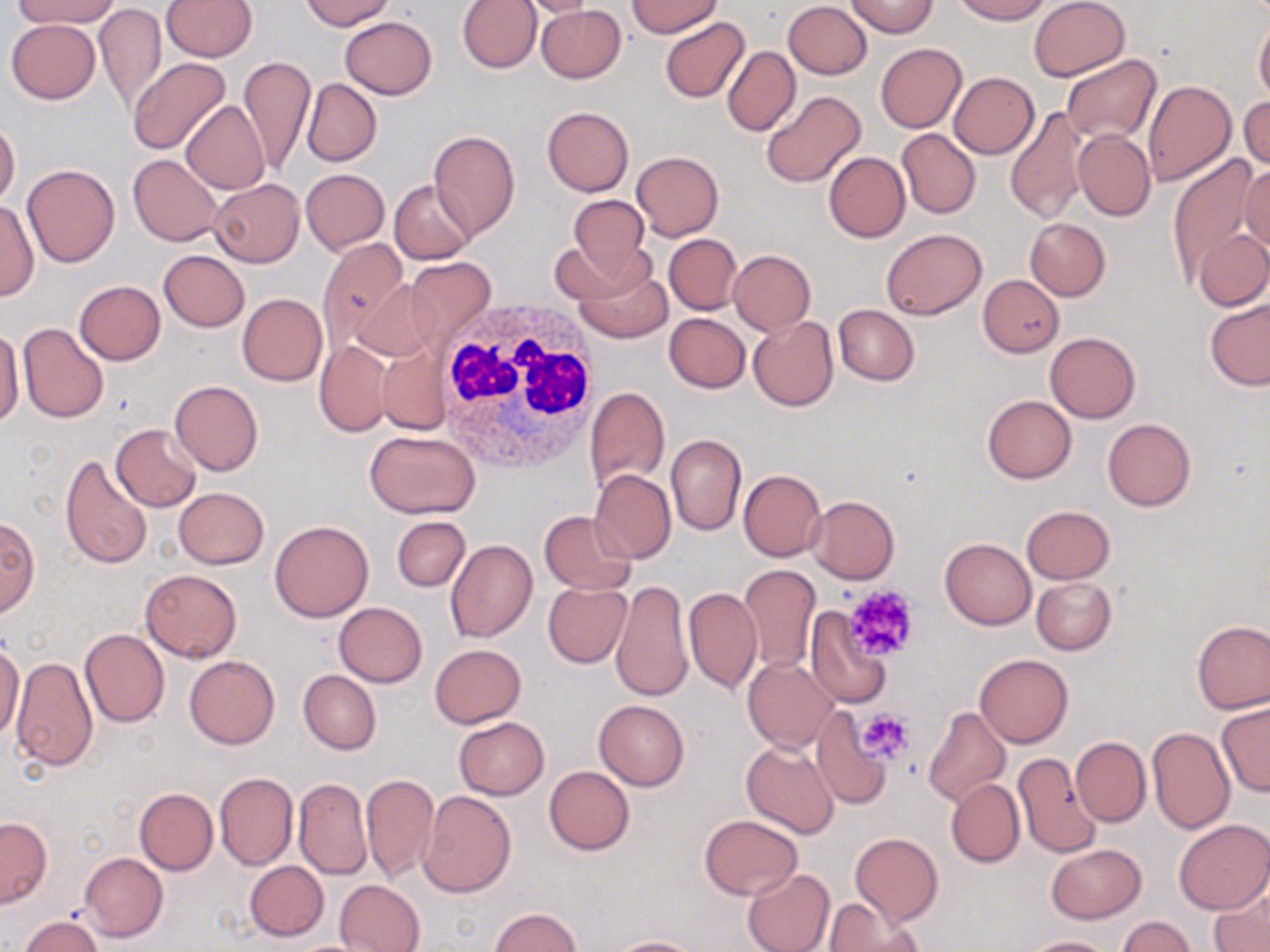
Approximate bounding boxes as [x1, y1, x2, y2] in pixels. Platelet locations: [842, 585, 920, 662], [857, 708, 914, 763]. Uninfected red blood cell locations: [13, 0, 118, 29], [162, 0, 257, 61], [302, 0, 393, 30], [457, 0, 541, 73], [518, 0, 603, 19], [627, 0, 722, 37], [952, 0, 1051, 23], [1028, 0, 1130, 82], [784, 1, 872, 79], [846, 1, 938, 37], [94, 3, 166, 113], [536, 5, 625, 82], [340, 17, 436, 99], [660, 17, 749, 103], [6, 18, 100, 103], [1255, 18, 1270, 105], [875, 43, 967, 133], [722, 46, 800, 137], [1059, 54, 1160, 145], [238, 55, 314, 175], [128, 57, 231, 156], [949, 72, 1039, 158], [302, 78, 382, 166], [1142, 79, 1237, 185], [761, 90, 866, 189], [1240, 94, 1269, 171], [182, 100, 269, 194], [1005, 106, 1091, 224], [542, 107, 634, 197], [0, 121, 20, 205], [897, 129, 980, 219], [428, 130, 520, 239], [1072, 130, 1155, 220], [632, 151, 723, 240], [823, 152, 910, 242], [129, 153, 225, 247], [1168, 158, 1258, 281], [1238, 159, 1269, 259], [22, 164, 120, 267], [301, 169, 389, 254], [210, 178, 304, 267], [390, 179, 476, 264], [566, 195, 651, 286], [0, 198, 38, 302], [1025, 218, 1110, 300], [882, 228, 985, 320], [1195, 229, 1270, 311], [664, 234, 741, 314], [318, 238, 407, 348], [549, 240, 634, 305], [159, 250, 248, 331], [728, 250, 815, 334], [404, 257, 495, 351], [575, 265, 671, 343], [978, 275, 1063, 356], [354, 278, 439, 360], [74, 281, 165, 364], [237, 293, 327, 386], [1204, 297, 1270, 390], [833, 305, 919, 386], [664, 312, 750, 392], [749, 316, 838, 411], [18, 323, 108, 422], [1, 324, 24, 426], [1044, 332, 1140, 422], [313, 339, 394, 437], [376, 347, 449, 434], [169, 379, 263, 476], [584, 386, 669, 492], [981, 395, 1076, 484], [1102, 419, 1195, 511], [110, 423, 201, 513], [364, 430, 480, 517], [666, 432, 746, 536], [60, 452, 152, 569], [738, 468, 826, 561], [589, 469, 676, 564], [173, 487, 269, 569], [805, 495, 900, 583], [1021, 505, 1115, 584], [540, 510, 636, 595], [392, 516, 470, 592], [0, 517, 40, 616], [270, 519, 373, 621], [940, 537, 1035, 629], [445, 539, 539, 642], [738, 564, 820, 674], [139, 569, 242, 661], [1031, 576, 1116, 655], [610, 580, 692, 702], [542, 581, 633, 668], [684, 586, 762, 695], [334, 602, 427, 687], [805, 610, 893, 709], [1193, 621, 1270, 713], [79, 628, 168, 728], [0, 637, 25, 745], [429, 644, 525, 727], [10, 654, 97, 771], [184, 654, 280, 749], [974, 654, 1074, 748], [742, 656, 840, 752], [298, 670, 381, 755], [594, 699, 689, 790], [1216, 702, 1269, 797], [923, 706, 1010, 808], [810, 708, 891, 808], [453, 716, 549, 799], [1147, 726, 1235, 833], [1070, 736, 1150, 826], [740, 739, 839, 839], [1012, 753, 1101, 859], [544, 765, 634, 854], [214, 772, 298, 869], [361, 773, 439, 882], [294, 778, 372, 880], [946, 778, 1024, 867], [134, 788, 218, 875], [420, 791, 517, 897], [699, 816, 800, 899], [0, 818, 51, 907], [1173, 819, 1270, 915], [850, 832, 943, 924], [1045, 844, 1146, 924], [80, 852, 167, 942], [245, 861, 328, 941], [742, 868, 835, 952], [334, 879, 424, 951], [1211, 882, 1270, 952], [826, 897, 925, 952], [489, 907, 581, 951], [19, 915, 102, 952], [1117, 916, 1195, 952], [607, 936, 707, 952], [1023, 936, 1115, 952]. White blood cell locations: [434, 301, 602, 475]. Slide-level diagnosis: negative for blood parasites. Thin blood film. Optical microscopy. 1000x magnification. May-Grünwald-Giemsa stain. Single field of view. Image is 1270×952 pixels.